Name the parasite shown.
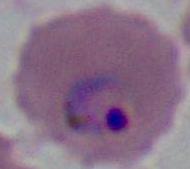

This is Plasmodium.

modality = photomicrograph
magnification = 400x or 1000x